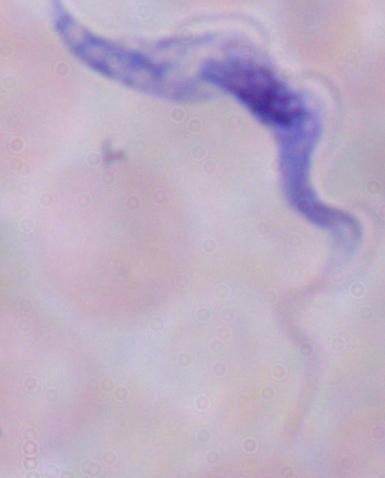
1000x magnification. A trypanosome is shown. Micrograph.